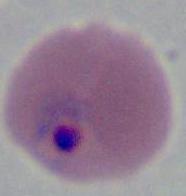
A Plasmodium parasite is shown. Micrograph. Captured at either 400x or 1000x magnification.